Locate and identify every blood parasite.
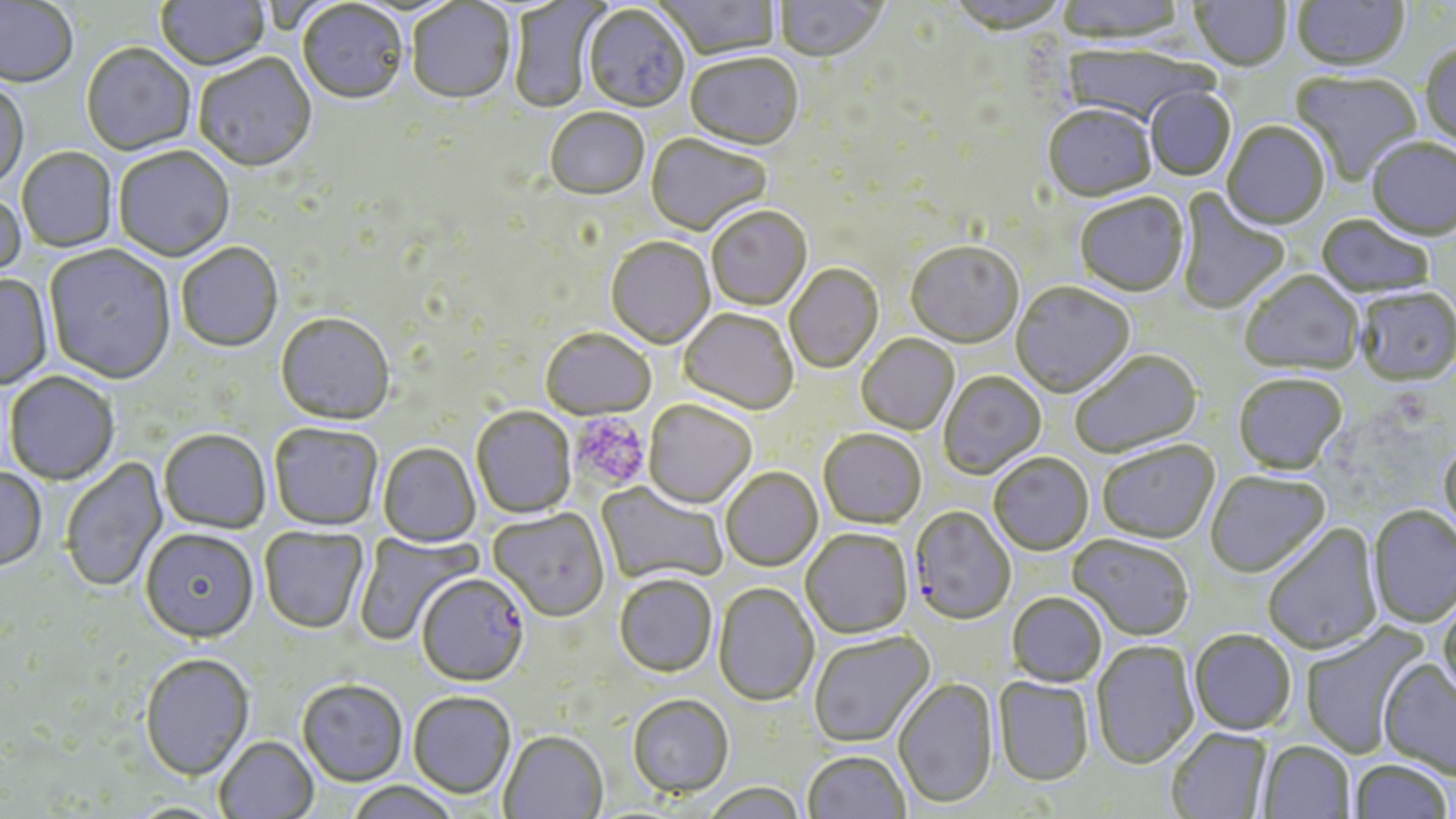
Approximate bounding boxes as (x1,y1)-(x2,y2) corner pairs in pixels.
Plasmodium falciparum-infected red blood cells: (909,507)-(1016,626), (416,576)-(529,689).
No Plasmodium ovale, Plasmodium malariae, Plasmodium vivax, Babesia divergens, or Trypanosoma brucei observed.

Summary:
  - Uninfected red blood cell locations: (156,0)-(270,72), (654,0)-(780,62), (946,0)-(1070,38), (1057,0)-(1186,46), (1191,0)-(1291,73), (1293,0)-(1409,74), (775,1)-(887,66), (0,2)-(78,90), (407,2)-(515,106), (509,2)-(606,114), (297,3)-(408,107), (583,6)-(690,115), (1420,44)-(1456,152), (1061,45)-(1211,127), (81,46)-(195,156), (194,55)-(317,175), (685,55)-(804,153), (1290,72)-(1423,188), (0,82)-(29,193), (1144,87)-(1235,182), (1042,106)-(1157,205), (545,110)-(649,202), (1222,122)-(1330,232), (645,135)-(772,237), (1367,139)-(1456,243), (114,148)-(235,263), (17,149)-(117,252), (1175,188)-(1291,316), (0,190)-(26,291), (1075,195)-(1189,299), (707,207)-(812,311), (1315,216)-(1435,300), (606,238)-(716,350), (177,244)-(284,353), (906,244)-(1023,349), (44,246)-(176,385), (785,265)-(884,374), (1240,272)-(1363,377), (0,275)-(53,391), (1011,283)-(1136,399), (1355,289)-(1456,388), (678,310)-(798,416), (276,315)-(395,427), (540,330)-(656,422), (856,335)-(960,436), (1070,350)-(1203,461), (937,372)-(1046,480), (4,373)-(119,486), (1233,375)-(1348,476), (643,401)-(756,510), (470,408)-(576,519), (269,425)-(383,532), (159,431)-(270,535), (818,431)-(927,530), (1438,439)-(1456,547), (1097,441)-(1220,545), (378,444)-(480,548), (989,455)-(1093,556), (61,457)-(168,593), (721,468)-(823,572), (0,469)-(47,573), (1205,471)-(1331,579), (595,482)-(728,586), (1368,506)-(1456,629), (488,510)-(609,624), (1262,524)-(1383,655), (259,528)-(368,635), (801,530)-(913,640), (140,531)-(259,646), (353,531)-(482,645), (1067,534)-(1193,642), (614,577)-(717,678), (713,583)-(819,708), (1006,593)-(1106,688), (1437,595)-(1456,707), (1300,622)-(1430,759), (1189,629)-(1297,736), (808,631)-(936,750), (1092,640)-(1199,768), (140,655)-(255,783), (1377,658)-(1456,777), (893,677)-(998,810), (993,678)-(1094,787), (297,681)-(407,788), (408,693)-(515,801), (628,697)-(733,801), (1166,728)-(1271,819), (499,733)-(608,819), (215,737)-(318,819), (1258,741)-(1355,818), (802,751)-(911,819), (1349,759)-(1452,818), (346,782)-(459,819), (701,784)-(807,819)
  - Platelet locations: (570,414)-(649,490)
  - Slide-level diagnosis: Plasmodium falciparum
  - Magnification: 1000x
  - Stain: May-Grünwald-Giemsa
  - Modality: optical microscopy
  - Field of view: one of a larger specimen
  - Image size: 1456×819 pixels
  - Preparation: thin blood film